Classify this cell by malaria status.
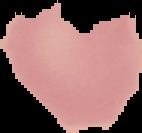
Uninfected.

Summary:
  - Image type: cell region segmented out of the field of view; surrounding area masked to black
  - Preparation: thin blood smear
  - Image size: 142×133 pixels